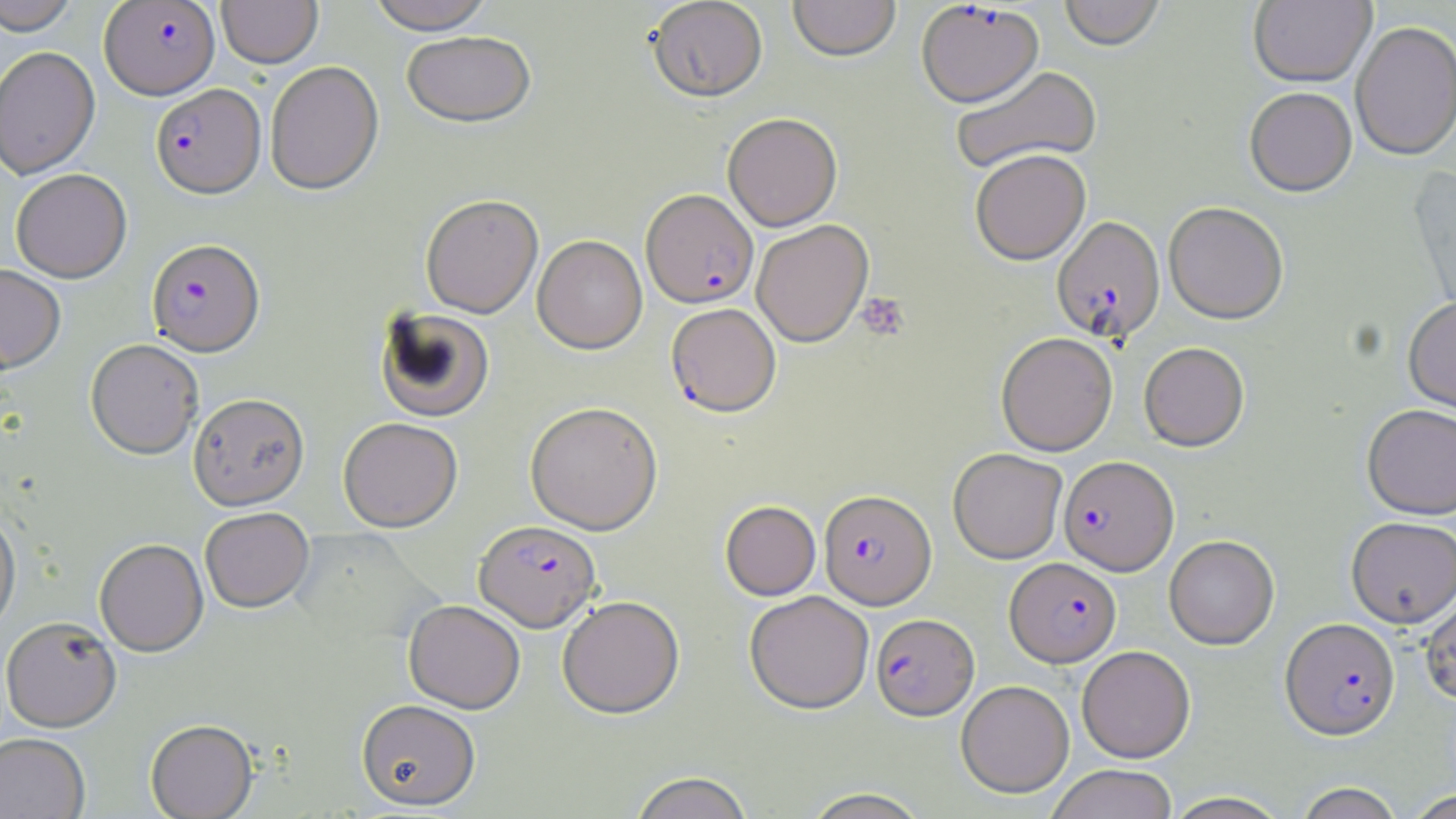

Approximate bounding boxes as (x1,y1)-(x2,y2) corner pairs in pixels. Plasmodium falciparum-infected red blood cell locations: (100,1)-(219,99), (916,2)-(1044,110), (151,83)-(265,198), (641,191)-(758,310), (1051,217)-(1165,344), (147,239)-(265,357), (666,304)-(781,418), (1059,456)-(1179,575), (819,490)-(937,610), (474,522)-(600,633), (1005,557)-(1121,667), (871,614)-(979,720), (1280,617)-(1400,739). Uninfected red blood cell locations: (0,0)-(80,35), (217,0)-(322,68), (366,0)-(495,35), (648,0)-(767,104), (788,0)-(901,64), (1059,0)-(1165,53), (1249,0)-(1376,88), (1351,21)-(1456,161), (402,33)-(537,131), (0,46)-(100,179), (265,61)-(383,195), (952,66)-(1103,175), (1245,87)-(1357,197), (723,114)-(842,232), (971,151)-(1090,266), (1407,166)-(1456,321), (11,168)-(132,283), (420,197)-(543,320), (1163,203)-(1288,325), (752,221)-(873,348), (533,236)-(647,355), (0,263)-(66,373), (1403,296)-(1456,416), (374,308)-(495,423), (996,333)-(1118,456), (85,339)-(204,460), (1139,342)-(1250,452), (188,394)-(310,512), (525,403)-(663,535), (1362,403)-(1456,520), (338,419)-(462,533), (948,448)-(1067,564), (720,501)-(821,601), (0,507)-(20,636), (200,509)-(314,614), (1346,517)-(1456,628), (1164,535)-(1279,650), (94,539)-(208,657), (1420,590)-(1456,705), (745,591)-(874,714), (557,597)-(685,719), (404,601)-(525,714), (1,617)-(121,732), (1077,645)-(1195,763), (956,680)-(1074,798), (357,701)-(480,812), (145,720)-(258,819), (0,733)-(90,818), (1046,764)-(1178,819), (629,772)-(755,819), (1293,782)-(1404,819), (800,787)-(932,819), (1405,790)-(1455,818), (1162,791)-(1291,819). Platelet locations: (856,293)-(909,341). Slide-level diagnosis: Plasmodium falciparum. Image is 1456×819 pixels. May-Grünwald-Giemsa-stained preparation. Single field of view. Thin blood smear. 1000x magnification. Light microscopy.